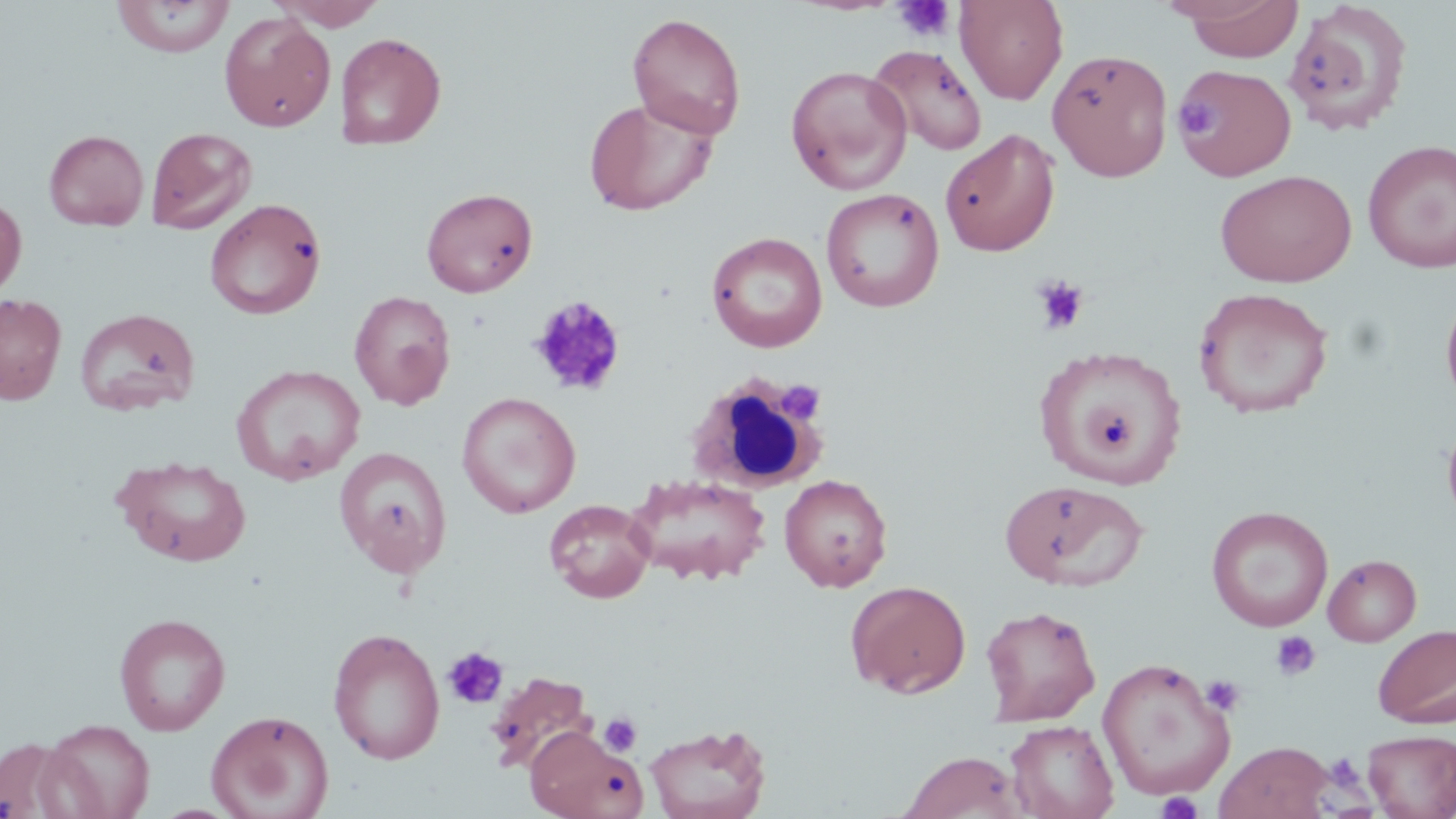
slide-level diagnosis = no evidence of blood parasites
modality = light microscopy
field of view = one of a larger specimen
platelet locations = approximate bounding boxes as [x1, y1, x2, y2] in pixels: [891, 0, 955, 41], [1175, 98, 1218, 140], [1031, 275, 1090, 334], [527, 295, 628, 396], [775, 379, 826, 426], [1271, 630, 1321, 681], [443, 646, 509, 709], [1201, 674, 1245, 717], [598, 712, 642, 757], [1324, 752, 1365, 793], [1156, 790, 1203, 819]
stain = May-Grünwald-Giemsa
preparation = thin blood smear
white blood cell locations = approximate bounding boxes as [x1, y1, x2, y2] in pixels: [686, 373, 830, 494]
uninfected red blood cell locations = approximate bounding boxes as [x1, y1, x2, y2] in pixels: [111, 0, 235, 58], [269, 0, 387, 30], [956, 0, 1068, 104], [1178, 0, 1304, 62], [1284, 1, 1414, 136], [219, 12, 336, 131], [627, 12, 747, 140], [335, 32, 446, 150], [868, 44, 988, 156], [1047, 48, 1174, 182], [1174, 63, 1296, 181], [786, 65, 912, 195], [584, 99, 717, 216], [146, 127, 257, 234], [43, 129, 149, 229], [940, 129, 1059, 256], [1362, 140, 1456, 273], [1215, 169, 1357, 287], [420, 187, 538, 297], [821, 188, 944, 312], [0, 192, 27, 302], [205, 198, 326, 320], [707, 231, 828, 353], [1440, 286, 1456, 415], [1193, 287, 1334, 418], [349, 290, 456, 410], [0, 293, 67, 404], [74, 307, 201, 415], [1035, 344, 1188, 489], [232, 364, 366, 486], [457, 392, 581, 518], [1441, 412, 1456, 533], [334, 446, 451, 576], [111, 454, 252, 567], [627, 473, 772, 585], [779, 473, 893, 592], [1000, 479, 1146, 592], [544, 499, 656, 603], [1207, 506, 1333, 632], [1323, 554, 1422, 646], [846, 579, 971, 698], [980, 605, 1101, 725], [113, 612, 231, 736], [1373, 623, 1456, 728], [327, 627, 445, 764], [1096, 657, 1236, 801], [483, 670, 599, 776], [206, 709, 334, 819], [39, 717, 156, 818], [1006, 720, 1119, 819], [644, 722, 771, 819], [526, 727, 647, 819], [1362, 730, 1456, 818], [0, 735, 83, 818], [1215, 741, 1333, 819], [898, 750, 1027, 819]
magnification = 1000x
image size = 1456×819 pixels